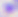
400x magnification. Micrograph. Toxoplasma gondii is seen.